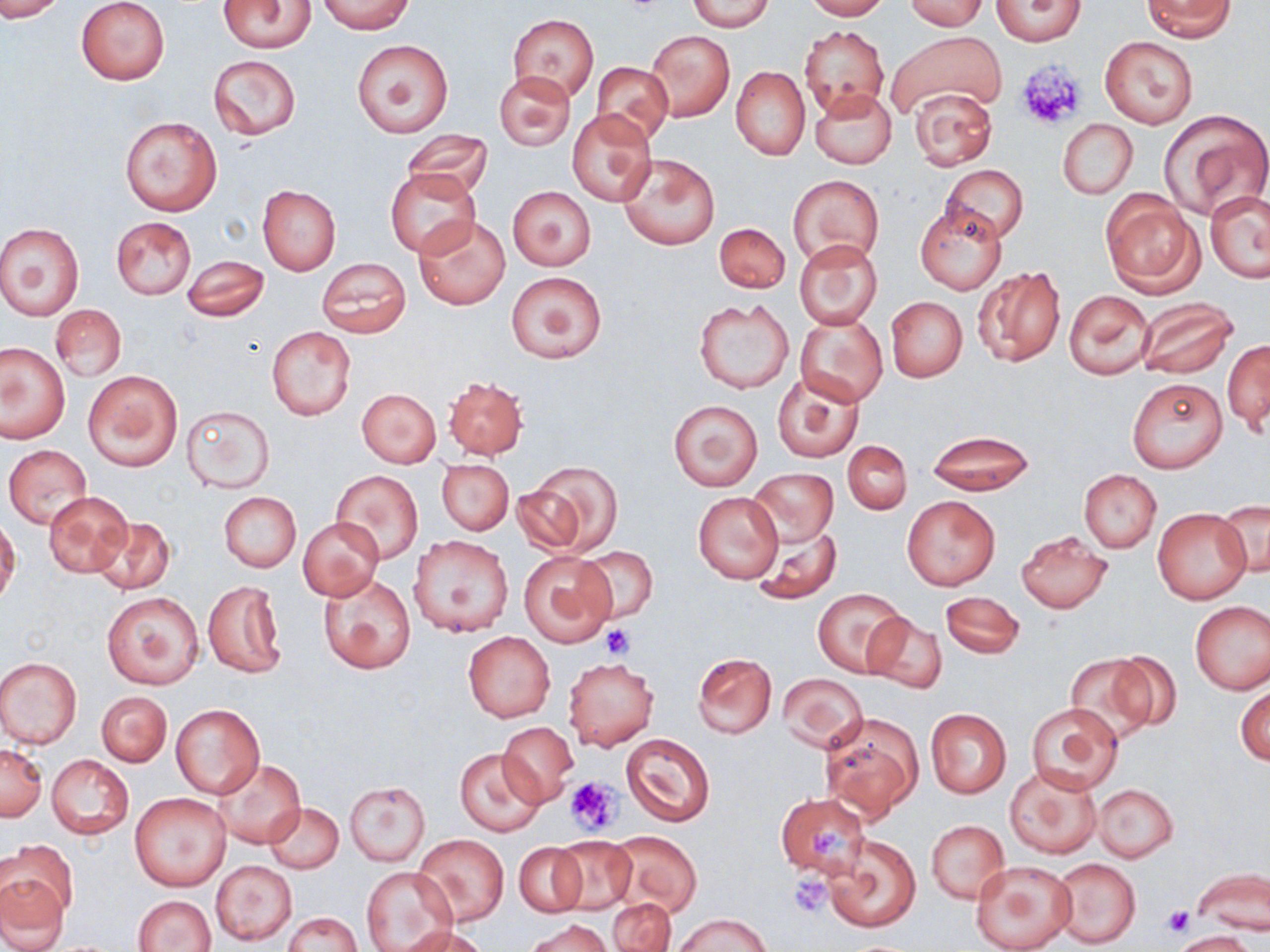

slide-level diagnosis = negative for blood parasites
image size = 1270×952 pixels
stain = May-Grünwald-Giemsa
field of view = one of a larger specimen
preparation = thin blood film
magnification = 1000x
uninfected red blood cell locations = approximate bounding boxes as named x1/y1/x2/y2 corners in pixels: (x1=0, y1=0, x2=64, y2=20), (x1=318, y1=0, x2=414, y2=33), (x1=687, y1=0, x2=774, y2=31), (x1=802, y1=0, x2=891, y2=20), (x1=902, y1=0, x2=989, y2=30), (x1=75, y1=1, x2=169, y2=84), (x1=219, y1=1, x2=317, y2=52), (x1=990, y1=1, x2=1084, y2=46), (x1=1143, y1=1, x2=1236, y2=40), (x1=507, y1=14, x2=598, y2=103), (x1=799, y1=25, x2=889, y2=121), (x1=885, y1=29, x2=1008, y2=118), (x1=646, y1=31, x2=734, y2=121), (x1=1100, y1=36, x2=1198, y2=128), (x1=353, y1=39, x2=453, y2=137), (x1=209, y1=54, x2=301, y2=142), (x1=591, y1=62, x2=674, y2=147), (x1=732, y1=68, x2=809, y2=160), (x1=495, y1=71, x2=575, y2=151), (x1=812, y1=88, x2=896, y2=168), (x1=910, y1=88, x2=996, y2=170), (x1=566, y1=110, x2=656, y2=207), (x1=1159, y1=110, x2=1270, y2=220), (x1=120, y1=114, x2=221, y2=216), (x1=1057, y1=119, x2=1137, y2=198), (x1=400, y1=129, x2=494, y2=200), (x1=617, y1=152, x2=720, y2=250), (x1=941, y1=165, x2=1029, y2=243), (x1=385, y1=168, x2=481, y2=257), (x1=789, y1=175, x2=884, y2=268), (x1=256, y1=185, x2=340, y2=276), (x1=508, y1=185, x2=595, y2=271), (x1=1204, y1=188, x2=1269, y2=284), (x1=1100, y1=192, x2=1201, y2=295), (x1=915, y1=204, x2=1008, y2=295), (x1=414, y1=215, x2=511, y2=310), (x1=112, y1=218, x2=196, y2=298), (x1=1, y1=222, x2=84, y2=319), (x1=714, y1=222, x2=790, y2=293), (x1=795, y1=240, x2=882, y2=328), (x1=182, y1=255, x2=269, y2=321), (x1=316, y1=257, x2=412, y2=338), (x1=974, y1=265, x2=1065, y2=368), (x1=506, y1=271, x2=607, y2=362), (x1=1065, y1=290, x2=1155, y2=377), (x1=886, y1=296, x2=967, y2=382), (x1=693, y1=299, x2=793, y2=393), (x1=1135, y1=299, x2=1237, y2=378), (x1=52, y1=304, x2=126, y2=382), (x1=795, y1=312, x2=888, y2=407), (x1=266, y1=325, x2=357, y2=421), (x1=1223, y1=340, x2=1269, y2=434), (x1=0, y1=342, x2=69, y2=443), (x1=83, y1=369, x2=183, y2=471), (x1=771, y1=371, x2=865, y2=462), (x1=443, y1=375, x2=529, y2=459), (x1=1126, y1=377, x2=1227, y2=472), (x1=357, y1=388, x2=441, y2=467), (x1=668, y1=399, x2=762, y2=491), (x1=181, y1=404, x2=276, y2=493), (x1=926, y1=431, x2=1034, y2=494), (x1=843, y1=440, x2=912, y2=514), (x1=4, y1=445, x2=92, y2=529), (x1=437, y1=460, x2=513, y2=535), (x1=520, y1=460, x2=625, y2=558), (x1=748, y1=467, x2=837, y2=547), (x1=331, y1=470, x2=424, y2=562), (x1=1079, y1=470, x2=1161, y2=552), (x1=42, y1=491, x2=134, y2=578), (x1=693, y1=491, x2=783, y2=583), (x1=218, y1=492, x2=300, y2=572), (x1=901, y1=493, x2=1001, y2=591), (x1=1217, y1=502, x2=1270, y2=577), (x1=1153, y1=508, x2=1252, y2=604), (x1=0, y1=515, x2=21, y2=605), (x1=89, y1=516, x2=174, y2=597), (x1=298, y1=517, x2=384, y2=599), (x1=751, y1=525, x2=841, y2=602), (x1=1016, y1=529, x2=1114, y2=613), (x1=410, y1=534, x2=513, y2=637), (x1=578, y1=546, x2=660, y2=622), (x1=518, y1=550, x2=616, y2=647), (x1=325, y1=557, x2=486, y2=658), (x1=319, y1=573, x2=416, y2=674), (x1=203, y1=580, x2=286, y2=678), (x1=813, y1=589, x2=907, y2=677), (x1=941, y1=590, x2=1024, y2=658), (x1=102, y1=592, x2=203, y2=689), (x1=1190, y1=600, x2=1270, y2=695), (x1=864, y1=613, x2=947, y2=692), (x1=464, y1=631, x2=555, y2=723), (x1=1105, y1=651, x2=1182, y2=732), (x1=693, y1=653, x2=776, y2=738), (x1=1065, y1=654, x2=1155, y2=742), (x1=0, y1=656, x2=82, y2=748), (x1=563, y1=656, x2=659, y2=751), (x1=777, y1=673, x2=868, y2=753), (x1=1236, y1=685, x2=1269, y2=765), (x1=97, y1=692, x2=170, y2=766), (x1=1025, y1=701, x2=1124, y2=794), (x1=171, y1=702, x2=265, y2=798), (x1=925, y1=708, x2=1012, y2=798), (x1=819, y1=711, x2=923, y2=820), (x1=498, y1=722, x2=577, y2=806), (x1=622, y1=733, x2=715, y2=826), (x1=0, y1=744, x2=45, y2=821), (x1=454, y1=748, x2=546, y2=836), (x1=47, y1=755, x2=133, y2=838), (x1=214, y1=758, x2=305, y2=850), (x1=1005, y1=764, x2=1103, y2=858), (x1=345, y1=783, x2=429, y2=865), (x1=1092, y1=783, x2=1179, y2=862), (x1=130, y1=792, x2=232, y2=892), (x1=775, y1=793, x2=870, y2=876), (x1=266, y1=802, x2=344, y2=873), (x1=926, y1=820, x2=1011, y2=904), (x1=610, y1=830, x2=702, y2=918), (x1=413, y1=833, x2=509, y2=926), (x1=824, y1=833, x2=919, y2=933), (x1=551, y1=836, x2=636, y2=914), (x1=1, y1=840, x2=76, y2=926), (x1=514, y1=842, x2=586, y2=916), (x1=1053, y1=858, x2=1140, y2=948), (x1=608, y1=859, x2=686, y2=944), (x1=970, y1=859, x2=1076, y2=952), (x1=212, y1=862, x2=297, y2=944), (x1=361, y1=865, x2=455, y2=952), (x1=1193, y1=866, x2=1270, y2=938), (x1=0, y1=870, x2=68, y2=952), (x1=135, y1=895, x2=215, y2=951), (x1=607, y1=898, x2=675, y2=951), (x1=283, y1=912, x2=360, y2=951), (x1=677, y1=914, x2=770, y2=952), (x1=527, y1=919, x2=615, y2=952), (x1=397, y1=926, x2=491, y2=951), (x1=1173, y1=932, x2=1256, y2=952)
platelet locations = approximate bounding boxes as named x1/y1/x2/y2 corners in pixels: (x1=1016, y1=59, x2=1088, y2=131), (x1=599, y1=623, x2=635, y2=658), (x1=565, y1=775, x2=623, y2=834), (x1=804, y1=824, x2=851, y2=860), (x1=790, y1=874, x2=833, y2=918), (x1=1164, y1=906, x2=1192, y2=936)
modality = light microscopy